Classify this cell by malaria status.
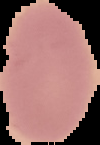
It is uninfected.

Image is 100×145 pixels. The area outside the segmented cell region is set to black. From a thin blood film.